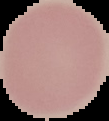 From a thin blood film. Cell region segmented out of the field of view; the surrounding area is masked to black. Malaria status: uninfected. Image is 109×121 pixels.